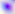
magnification = 400x
identification = Toxoplasma gondii
modality = micrograph